Give the preparation type.
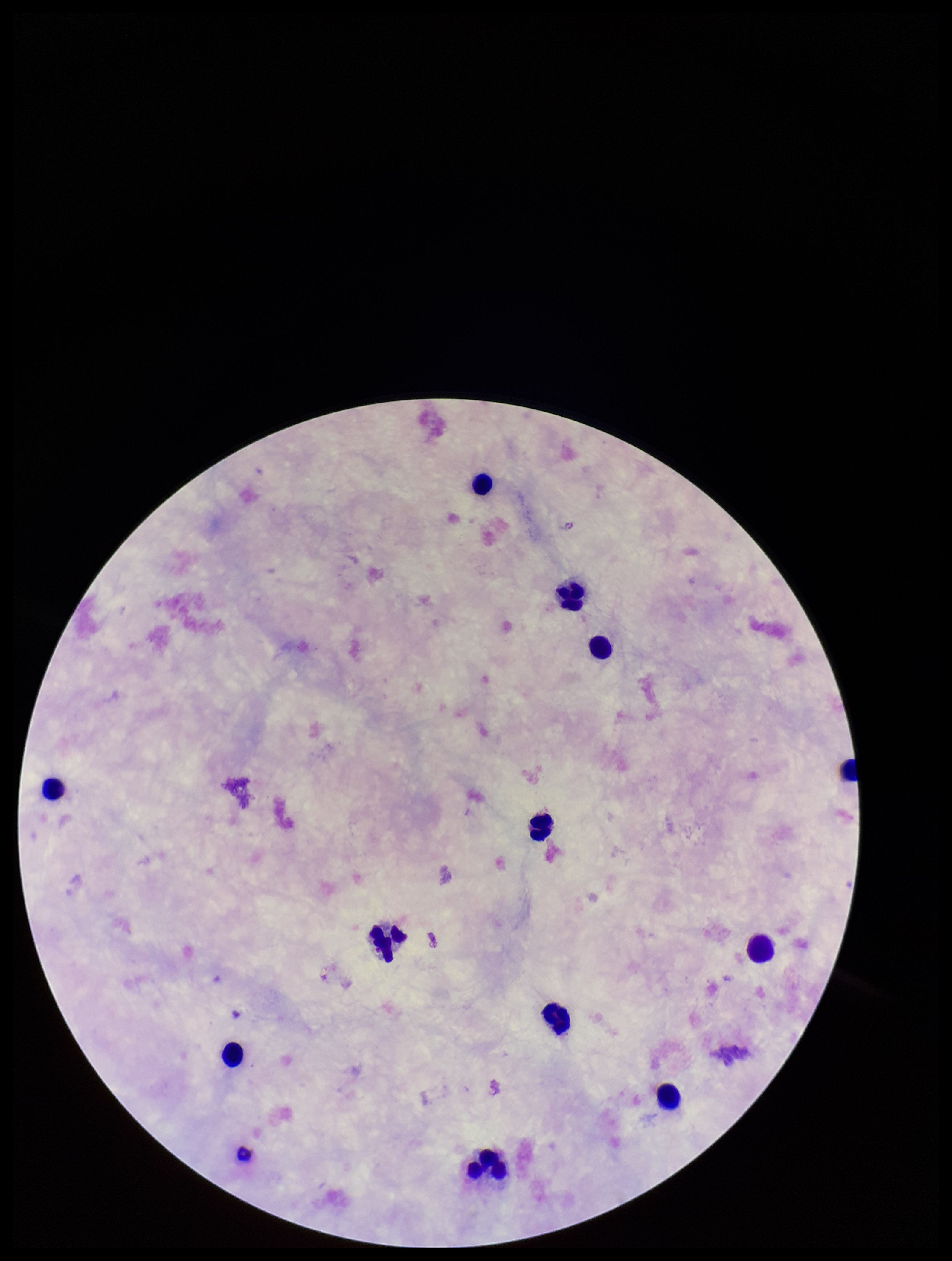

A thick smear.

Summary:
  - Field of view: one from this slide
  - Leukocyte count: 12
  - Stain: Giemsa
  - Parasite count: 0
  - Patient malaria status: negative
  - Image size: 952×1261 pixels
  - Plasmodium parasites: none detected
  - Capture: smartphone photograph through the microscope eyepiece